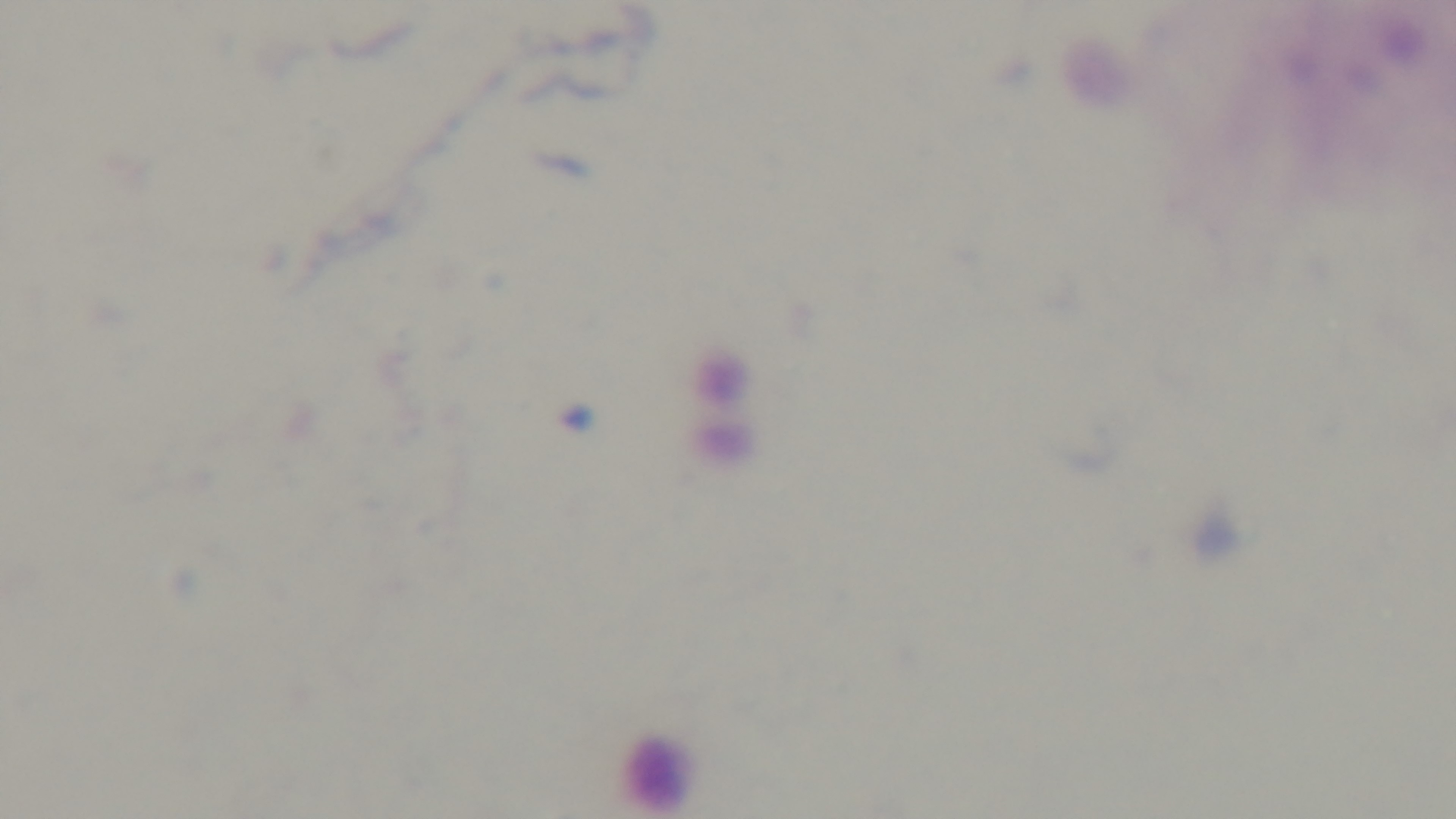 Giemsa stain. Oil-immersion objective, 100x. Preparation: thick blood film. Malaria status: negative. Photomicrograph. Captured with a mounted 4K digital camera. One field from the slide.